Report the malaria status of this cell.
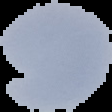

It is uninfected.

{
  "image_size": "112×112 pixels",
  "image_type": "segmented cell region with the area outside set to black",
  "preparation": "thin blood smear"
}